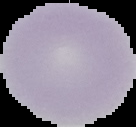

malaria status = uninfected
image type = segmented cell region on a black background
image size = 136×127 pixels
preparation = thin blood film